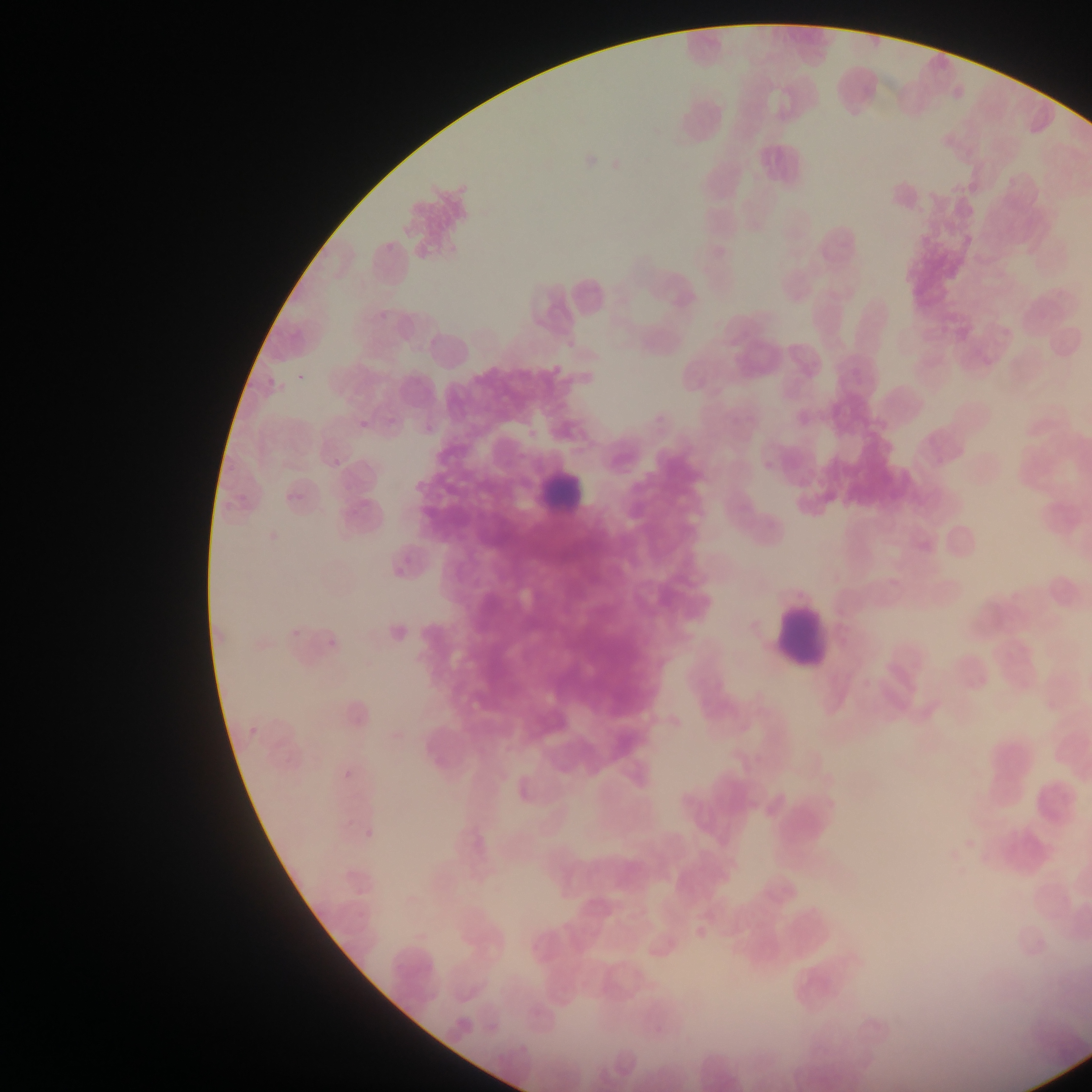
image size = 1092×1092 pixels
field of view = single
preparation = thin blood film
leukocyte locations = approximate bounding boxes as (left, top, right, bottom) in pixels: (537, 457, 590, 518), (775, 605, 828, 668)
malaria parasite locations = approximate bounding boxes as (left, top, right, bottom) in pixels: (375, 309, 387, 321), (384, 414, 398, 425), (357, 418, 374, 431), (758, 455, 778, 473), (326, 459, 338, 468), (288, 621, 303, 637), (323, 636, 339, 653), (246, 722, 266, 738), (338, 747, 358, 789), (362, 819, 386, 839), (689, 913, 714, 942)
capture = mobile-phone photograph through a microscope
country = Ghana